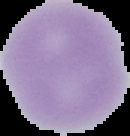 Segmented cell region on a black background. Malaria status: uninfected. Image is 130×136 pixels. From a thin blood film.